Locate every blood parasite and identify its species.
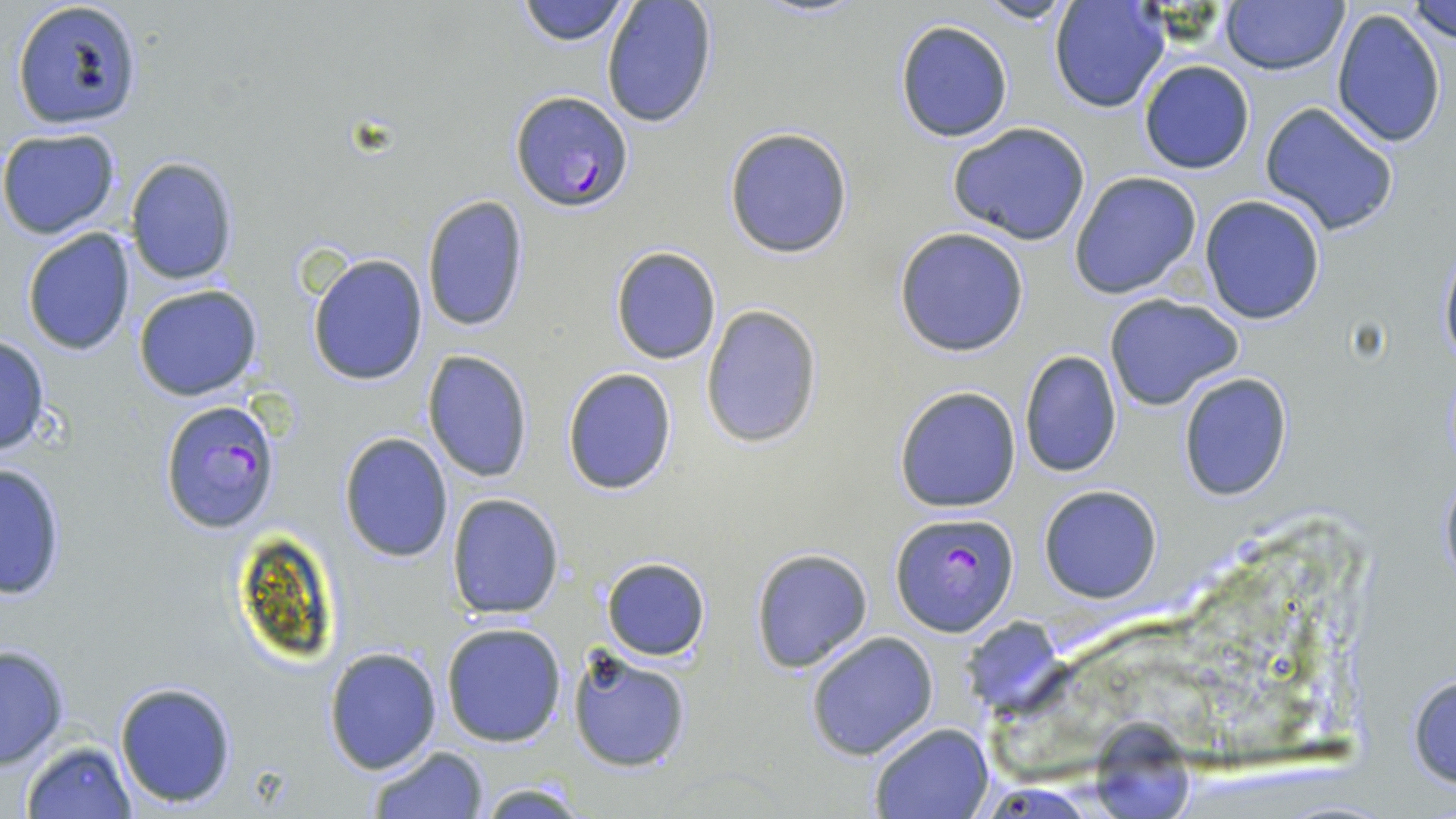

Approximate bounding boxes as named x1/y1/x2/y2 corners in pixels.
Plasmodium falciparum-infected red blood cells: (x1=510, y1=89, x2=633, y2=211), (x1=157, y1=399, x2=283, y2=537), (x1=889, y1=512, x2=1018, y2=637).
No Plasmodium ovale, Plasmodium malariae, Plasmodium vivax, Babesia divergens, or Trypanosoma brucei observed.

Summary:
  - Uninfected red blood cell locations: (x1=10, y1=0, x2=145, y2=132), (x1=515, y1=0, x2=633, y2=47), (x1=975, y1=0, x2=1075, y2=25), (x1=1221, y1=0, x2=1348, y2=76), (x1=1409, y1=0, x2=1456, y2=41), (x1=600, y1=1, x2=719, y2=129), (x1=1048, y1=1, x2=1170, y2=113), (x1=1331, y1=8, x2=1447, y2=149), (x1=894, y1=19, x2=1015, y2=143), (x1=1138, y1=60, x2=1254, y2=174), (x1=1260, y1=101, x2=1400, y2=237), (x1=947, y1=122, x2=1094, y2=246), (x1=723, y1=126, x2=854, y2=259), (x1=0, y1=128, x2=121, y2=240), (x1=124, y1=157, x2=239, y2=287), (x1=1068, y1=170, x2=1203, y2=300), (x1=421, y1=195, x2=531, y2=335), (x1=1199, y1=196, x2=1326, y2=324), (x1=894, y1=226, x2=1030, y2=357), (x1=21, y1=227, x2=137, y2=357), (x1=1437, y1=243, x2=1456, y2=373), (x1=611, y1=245, x2=721, y2=365), (x1=308, y1=254, x2=428, y2=387), (x1=134, y1=284, x2=264, y2=402), (x1=1102, y1=294, x2=1242, y2=412), (x1=700, y1=304, x2=825, y2=450), (x1=0, y1=335, x2=51, y2=456), (x1=422, y1=348, x2=535, y2=484), (x1=1020, y1=350, x2=1122, y2=477), (x1=561, y1=366, x2=678, y2=497), (x1=1178, y1=372, x2=1292, y2=501), (x1=893, y1=384, x2=1022, y2=514), (x1=338, y1=432, x2=453, y2=561), (x1=0, y1=461, x2=68, y2=601), (x1=1436, y1=471, x2=1456, y2=591), (x1=1038, y1=484, x2=1163, y2=604), (x1=446, y1=493, x2=565, y2=620), (x1=749, y1=546, x2=873, y2=673), (x1=601, y1=556, x2=710, y2=661), (x1=962, y1=618, x2=1066, y2=717), (x1=440, y1=623, x2=567, y2=748), (x1=805, y1=631, x2=939, y2=761), (x1=0, y1=643, x2=71, y2=770), (x1=322, y1=645, x2=444, y2=775), (x1=569, y1=646, x2=692, y2=774), (x1=1408, y1=666, x2=1456, y2=791), (x1=113, y1=679, x2=238, y2=810), (x1=1098, y1=715, x2=1193, y2=819), (x1=869, y1=723, x2=993, y2=818), (x1=18, y1=740, x2=138, y2=818), (x1=365, y1=745, x2=490, y2=818), (x1=470, y1=782, x2=595, y2=817)
  - Slide-level diagnosis: Plasmodium falciparum
  - Field of view: one of a larger specimen
  - Modality: light microscopy
  - Image size: 1456×819 pixels
  - Magnification: 1000x
  - Preparation: thin blood smear
  - Stain: May-Grünwald-Giemsa